Assess this cell for malaria.
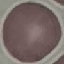
Uninfected.

stain = Giemsa
capture = smartphone camera at the microscope eyepiece
preparation = thin blood film
image type = automatically extracted cell patch, resized to 64 × 64 pixels